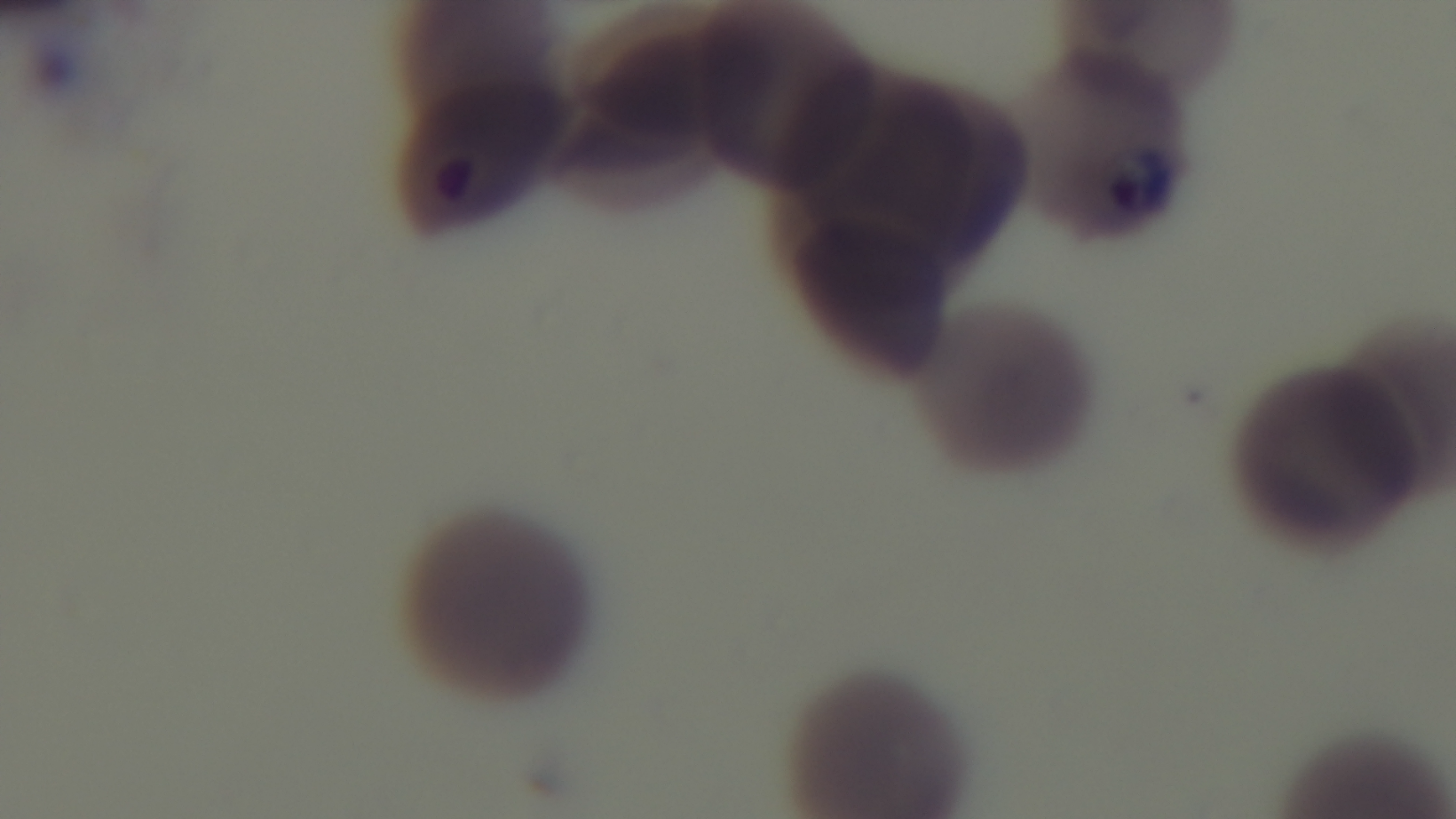
Light microscopy. Mounted 4K digital camera. Malaria status: positive. Preparation: thin. Giemsa stain. One field from the slide. 100x oil-immersion objective.